State which parasite is depicted.
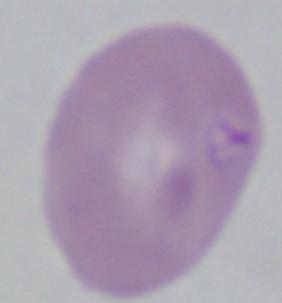

This is Babesia.

Micrograph. 1000x magnification.